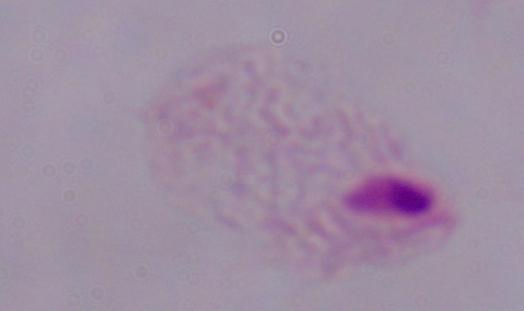 Captured at 1000x magnification. Photomicrograph. A trichomonad is shown.